Report the malaria status of this cell.
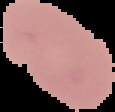

It is uninfected.

image size = 115×112 pixels
preparation = thin blood smear
image type = cell region segmented out of the field of view; surrounding area masked to black